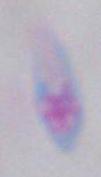

Summary:
  - Identification: Toxoplasma gondii
  - Magnification: 1000x
  - Modality: micrograph